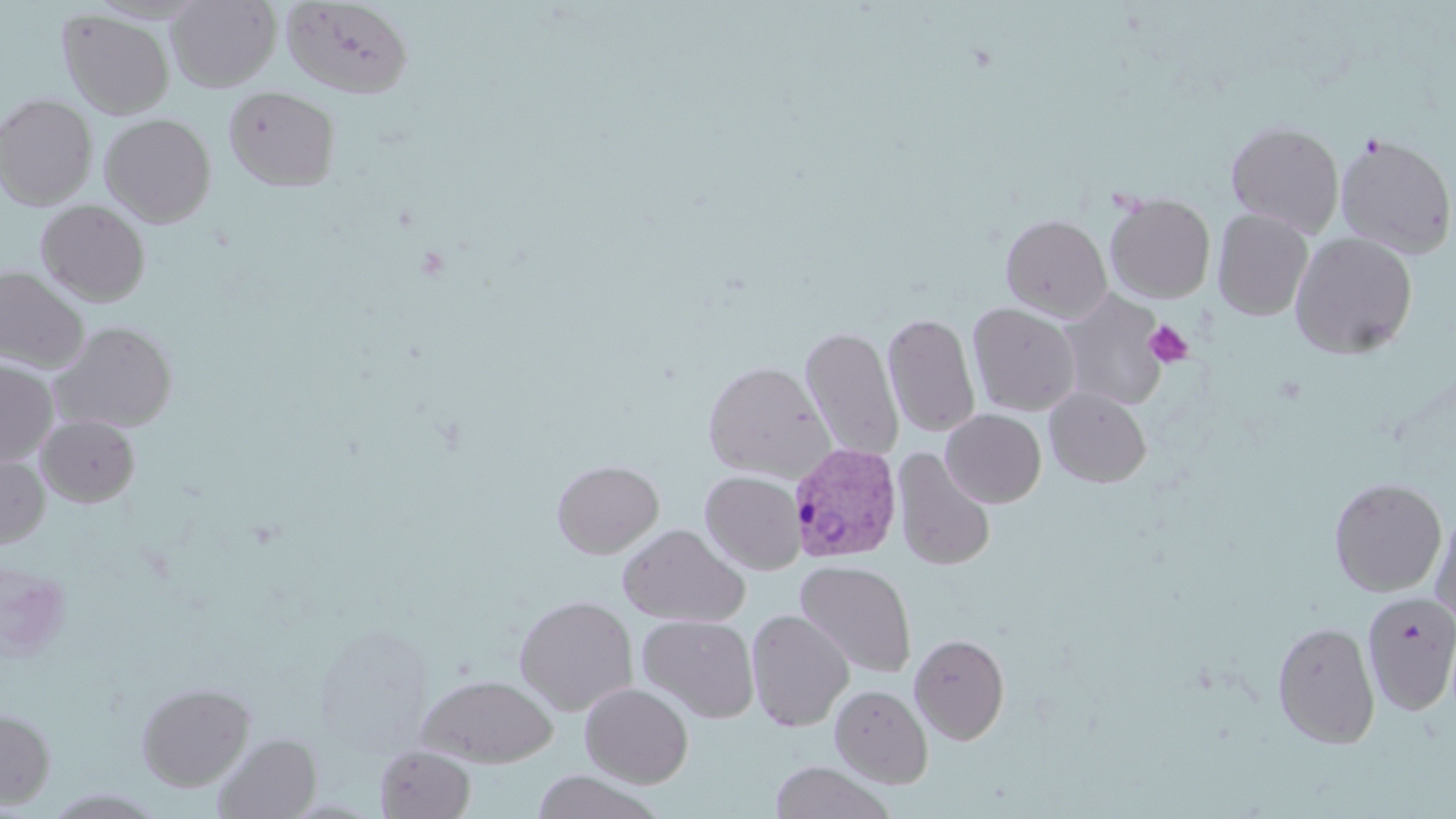

Summary:
  - Coordinate format: approximate bounding boxes as named x1/y1/x2/y2 corners in pixels
  - Uninfected red blood cell locations: (x1=168, y1=0, x2=280, y2=91), (x1=281, y1=0, x2=414, y2=99), (x1=58, y1=10, x2=174, y2=119), (x1=224, y1=86, x2=340, y2=192), (x1=0, y1=93, x2=97, y2=209), (x1=100, y1=113, x2=216, y2=227), (x1=1226, y1=120, x2=1345, y2=236), (x1=1335, y1=131, x2=1456, y2=259), (x1=1105, y1=192, x2=1215, y2=304), (x1=36, y1=200, x2=150, y2=306), (x1=1212, y1=209, x2=1313, y2=321), (x1=1000, y1=214, x2=1112, y2=321), (x1=1290, y1=232, x2=1418, y2=360), (x1=0, y1=266, x2=89, y2=372), (x1=1060, y1=290, x2=1170, y2=411), (x1=967, y1=302, x2=1081, y2=416), (x1=888, y1=304, x2=984, y2=570), (x1=883, y1=313, x2=980, y2=438), (x1=52, y1=322, x2=177, y2=433), (x1=800, y1=326, x2=903, y2=462), (x1=0, y1=359, x2=58, y2=468), (x1=702, y1=360, x2=835, y2=482), (x1=1045, y1=387, x2=1151, y2=487), (x1=941, y1=409, x2=1046, y2=507), (x1=37, y1=415, x2=140, y2=507), (x1=892, y1=448, x2=996, y2=571), (x1=0, y1=452, x2=49, y2=550), (x1=552, y1=459, x2=663, y2=558), (x1=700, y1=470, x2=805, y2=575), (x1=1329, y1=477, x2=1447, y2=596), (x1=1348, y1=478, x2=1451, y2=707), (x1=1430, y1=506, x2=1456, y2=627), (x1=618, y1=523, x2=749, y2=627), (x1=795, y1=560, x2=916, y2=678), (x1=0, y1=563, x2=72, y2=660), (x1=1361, y1=591, x2=1456, y2=716), (x1=515, y1=595, x2=638, y2=715), (x1=746, y1=609, x2=853, y2=732), (x1=637, y1=615, x2=759, y2=723), (x1=1272, y1=620, x2=1380, y2=749), (x1=910, y1=633, x2=1010, y2=745), (x1=415, y1=674, x2=558, y2=766), (x1=136, y1=681, x2=255, y2=791), (x1=580, y1=682, x2=694, y2=788), (x1=830, y1=684, x2=933, y2=788), (x1=0, y1=708, x2=56, y2=808), (x1=214, y1=733, x2=321, y2=819), (x1=375, y1=745, x2=476, y2=818), (x1=770, y1=761, x2=893, y2=819), (x1=530, y1=771, x2=663, y2=819)
  - Platelet locations: (x1=1145, y1=320, x2=1193, y2=366)
  - Plasmodium vivax-infected red blood cell locations: (x1=788, y1=441, x2=903, y2=563)
  - Slide-level diagnosis: Plasmodium vivax
  - Preparation: thin blood smear
  - Modality: light microscopy
  - Field of view: one of a larger specimen
  - Magnification: 1000x
  - Image size: 1456×819 pixels
  - Stain: May-Grünwald-Giemsa